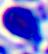

Summary:
  - Magnification: 400x
  - Identification: leukocyte
  - Modality: photomicrograph